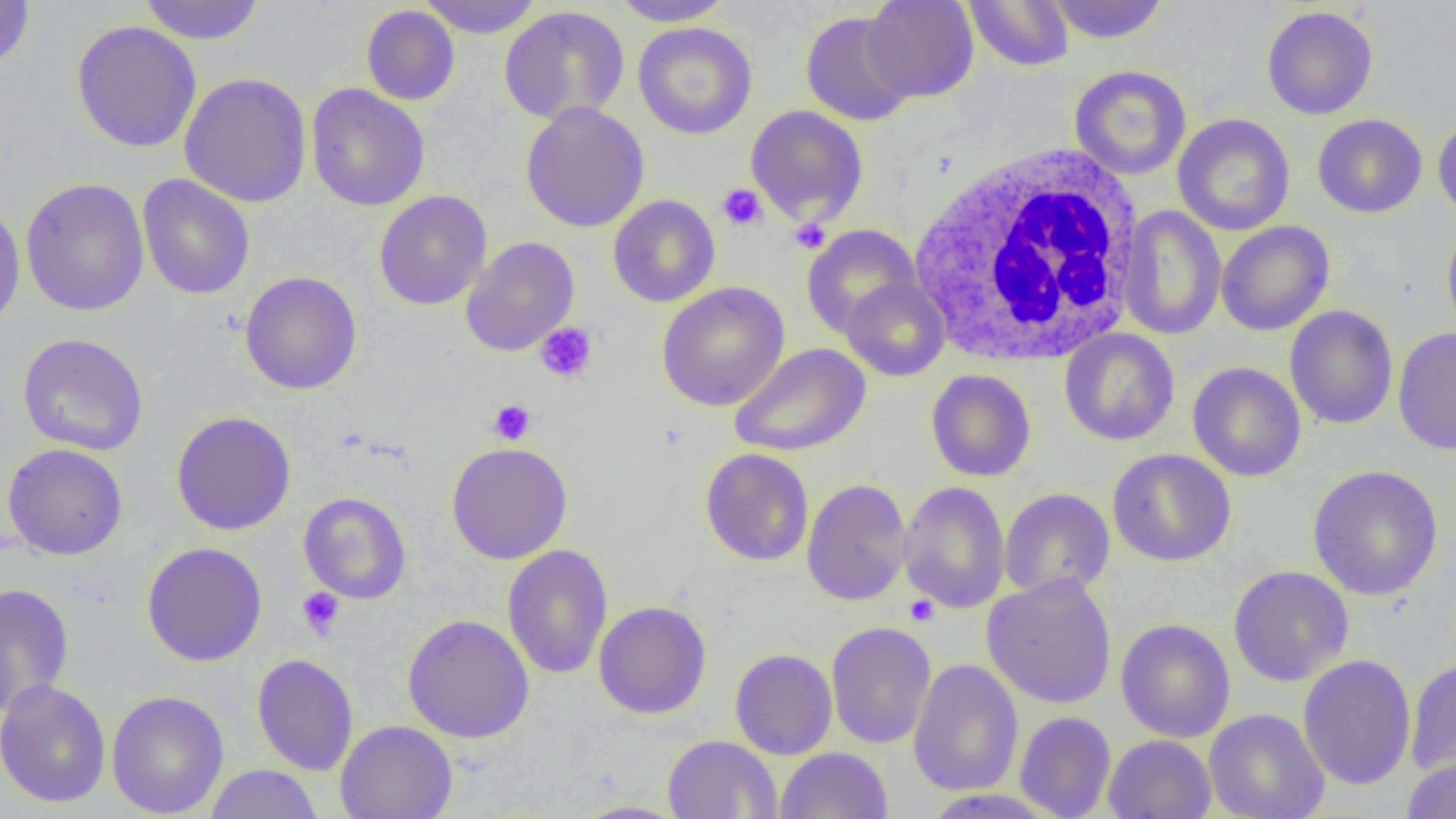
Approximate bounding boxes as (x1,y1)-(x2,y2) corner pairs in pixels. White blood cell locations: (908,144)-(1148,366). Platelet locations: (717,184)-(767,232), (788,218)-(832,253), (534,322)-(597,383), (488,399)-(536,445), (297,587)-(345,639), (904,594)-(939,626). Uninfected red blood cell locations: (1,0)-(35,72), (138,0)-(265,45), (417,0)-(543,38), (611,0)-(734,27), (862,0)-(979,102), (1045,0)-(1169,45), (964,1)-(1075,71), (361,4)-(461,106), (499,6)-(630,125), (1261,6)-(1378,120), (800,12)-(917,126), (71,21)-(202,153), (633,22)-(757,140), (1069,65)-(1191,180), (179,72)-(312,208), (305,83)-(431,212), (520,102)-(649,233), (744,105)-(869,226), (1172,113)-(1296,236), (1433,113)-(1456,225), (1312,114)-(1427,218), (137,174)-(255,300), (20,177)-(150,317), (374,190)-(492,310), (607,194)-(720,308), (0,202)-(26,330), (1118,206)-(1226,340), (1442,219)-(1456,340), (1215,220)-(1335,336), (801,224)-(922,339), (461,236)-(580,357), (239,271)-(362,395), (840,277)-(950,381), (656,282)-(790,412), (1284,305)-(1398,430), (1393,327)-(1456,455), (1059,328)-(1180,446), (17,332)-(149,456), (728,343)-(871,457), (1187,361)-(1306,482), (925,369)-(1036,482), (171,411)-(296,536), (446,442)-(572,564), (3,443)-(128,560), (700,448)-(814,566), (1107,448)-(1236,567), (1307,464)-(1443,600), (801,478)-(912,606), (898,481)-(1011,614), (999,488)-(1115,600), (298,491)-(412,604), (141,542)-(267,667), (502,544)-(613,680), (1228,566)-(1354,687), (981,573)-(1118,709), (0,582)-(75,715), (593,601)-(711,719), (402,614)-(534,743), (1115,618)-(1236,742), (826,621)-(936,749), (729,648)-(837,759), (252,654)-(358,775), (1298,654)-(1416,791), (907,658)-(1024,796), (1405,659)-(1456,777), (0,679)-(111,808), (106,690)-(229,818), (1204,708)-(1330,819), (1014,711)-(1116,818), (335,720)-(457,819), (1103,734)-(1217,819), (662,735)-(782,818), (775,747)-(893,818), (1402,755)-(1456,819), (204,764)-(323,819), (917,789)-(1059,817), (569,800)-(689,818). Slide-level diagnosis: no evidence of blood parasites. Thin blood film. Captured at 1000x magnification. Single field of view. Light microscopy. Image is 1456×819 pixels.